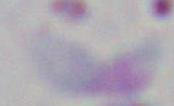
Summary:
  - Modality: micrograph
  - Magnification: 1000x
  - Identification: Toxoplasma gondii